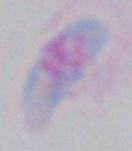
modality: micrograph
identification: Toxoplasma gondii
magnification: 1000x